Classify this cell by malaria status.
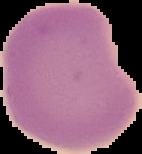

It is uninfected.

Image is 142×154 pixels. Cell region segmented out of the field of view; the surrounding area is masked to black. From a thin blood smear.